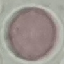

{
  "result": "no malaria parasites detected",
  "capture": "smartphone through the microscope eyepiece",
  "preparation": "thin blood smear",
  "stain": "Giemsa",
  "image_type": "cell patch, automatically extracted from a larger field of view and resized to 64 × 64 pixels"
}